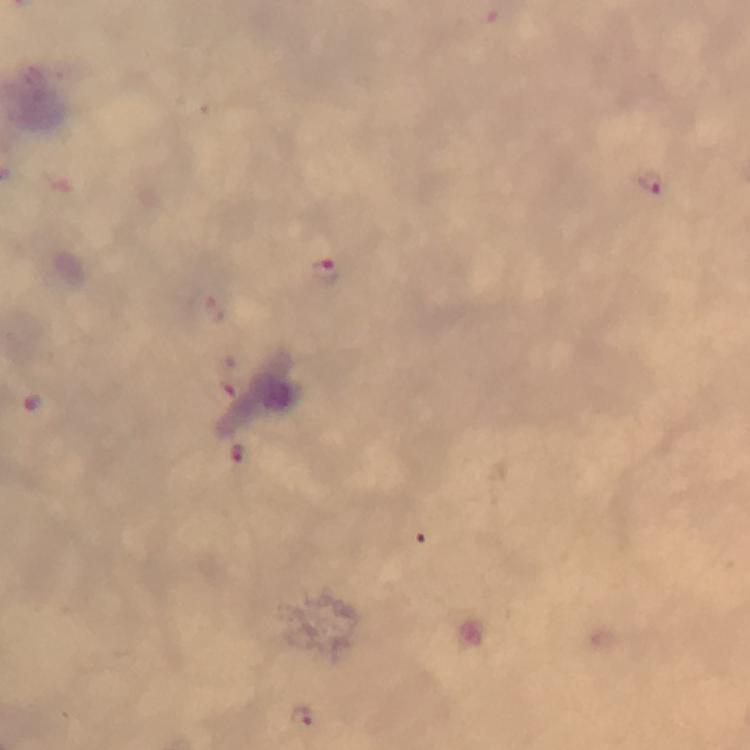 Approximate centers as {x, y} in pixels. Plasmodium parasite locations: {653, 184}, {326, 274}, {220, 390}, {31, 402}, {238, 453}, {303, 717}. Cropped region of a single field of view. Image is 750×750 pixels. Thick smear. At 100x magnification. Photographed with a smartphone mounted on the microscope. From a diagnostic examination for malaria. Giemsa-stained preparation. Immersion oil was used.